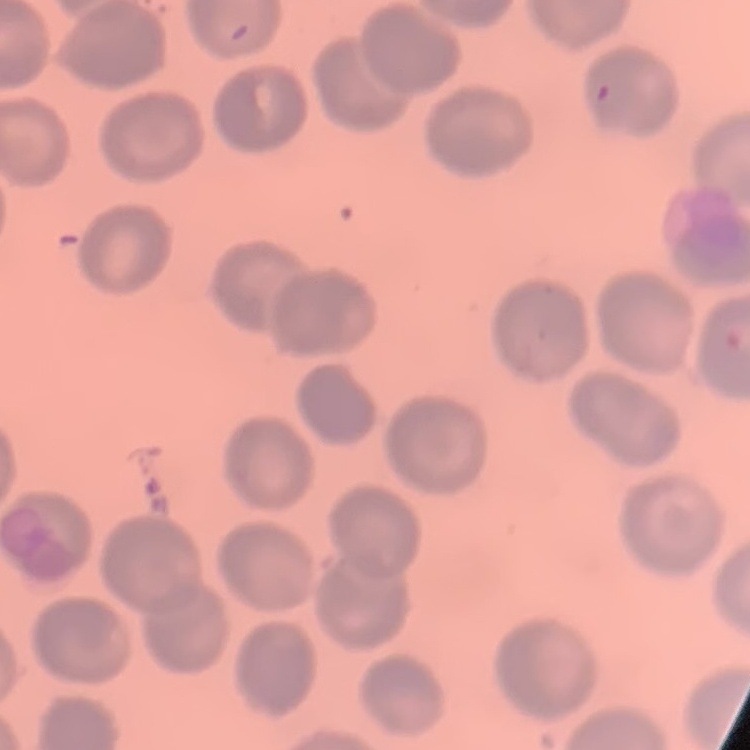

erythrocyte morphology = no rouleaux formation
stain = Field's or Giemsa
image type = one tile cut from a larger photomicrograph
preparation = thin peripheral smear